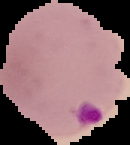
{
  "image_size": "130×145 pixels",
  "malaria_status": "parasitized",
  "image_type": "segmented cell region on a black background",
  "preparation": "thin blood smear"
}